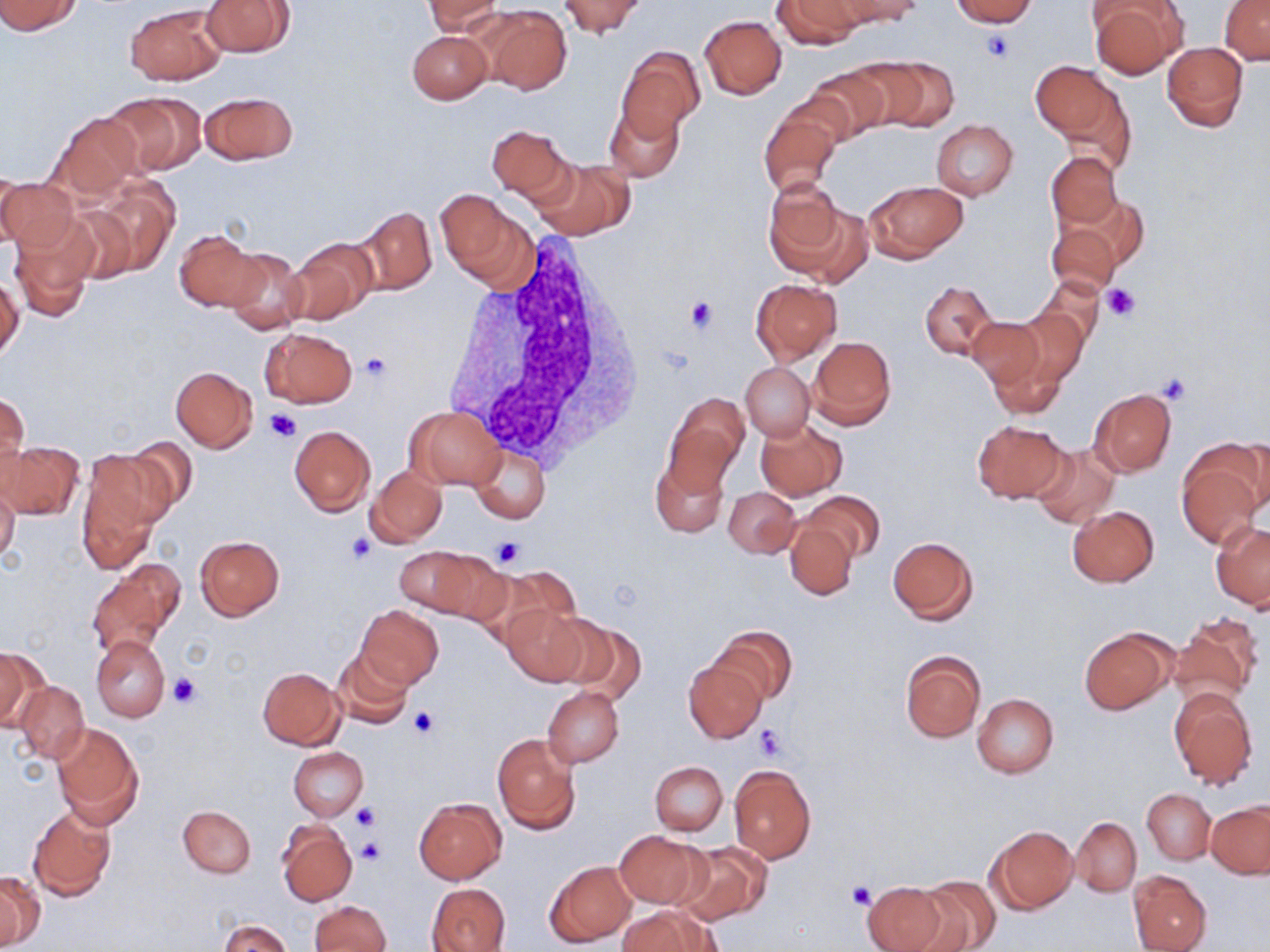

Summary:
  - Coordinate format: approximate bounding boxes as (x1, y1, x2, y2) in pixels
  - Uninfected red blood cell locations: (0, 0, 83, 35), (199, 0, 294, 57), (425, 0, 503, 37), (560, 0, 644, 37), (773, 0, 864, 48), (838, 0, 924, 26), (950, 0, 1037, 26), (1087, 1, 1185, 80), (1219, 1, 1270, 64), (125, 3, 227, 85), (482, 6, 570, 93), (698, 15, 786, 100), (406, 30, 491, 105), (1161, 42, 1248, 132), (617, 48, 704, 140), (857, 58, 957, 130), (1031, 61, 1118, 140), (804, 66, 889, 141), (1056, 74, 1139, 173), (102, 90, 206, 175), (198, 90, 298, 166), (604, 101, 683, 183), (758, 108, 840, 199), (48, 112, 143, 200), (930, 119, 1019, 200), (486, 123, 574, 203), (1046, 151, 1122, 230), (534, 159, 634, 240), (0, 173, 77, 257), (88, 179, 179, 274), (764, 180, 846, 276), (864, 180, 966, 262), (436, 189, 533, 287), (61, 203, 138, 286), (353, 206, 437, 295), (1046, 214, 1126, 297), (9, 216, 96, 322), (177, 230, 264, 314), (284, 237, 377, 327), (219, 244, 309, 335), (0, 275, 23, 364), (1032, 278, 1107, 349), (751, 279, 842, 362), (921, 280, 997, 361), (1009, 308, 1087, 387), (966, 317, 1044, 388), (260, 328, 357, 408), (809, 336, 896, 430), (986, 342, 1068, 420), (742, 363, 813, 440), (170, 367, 258, 452), (1088, 387, 1176, 477), (1, 390, 29, 482), (665, 394, 749, 490), (406, 405, 505, 490), (756, 419, 847, 499), (971, 420, 1068, 503), (288, 425, 375, 516), (124, 436, 200, 516), (1227, 439, 1270, 516), (2, 441, 84, 519), (1029, 442, 1121, 528), (471, 445, 550, 524), (77, 449, 165, 568), (1177, 451, 1265, 551), (650, 455, 728, 536), (365, 466, 447, 548), (0, 479, 20, 566), (724, 486, 800, 558), (802, 490, 883, 565), (1067, 505, 1160, 588), (785, 520, 856, 599), (1212, 522, 1269, 610), (194, 535, 285, 621), (887, 535, 979, 624), (394, 546, 488, 616), (426, 553, 512, 629), (89, 562, 181, 654), (481, 567, 580, 649), (356, 604, 444, 689), (501, 604, 588, 685), (551, 615, 644, 701), (1169, 616, 1261, 707), (710, 626, 797, 704), (1079, 627, 1175, 713), (91, 635, 171, 722), (0, 645, 41, 730), (333, 650, 415, 728), (900, 651, 985, 742), (685, 659, 767, 742), (257, 666, 345, 749), (15, 681, 90, 765), (543, 686, 623, 767), (1168, 686, 1257, 790), (972, 693, 1059, 778), (50, 722, 144, 827), (492, 733, 581, 835), (289, 746, 368, 821), (650, 760, 727, 835), (729, 765, 815, 863), (1143, 788, 1215, 863), (415, 798, 506, 883), (1206, 801, 1270, 879), (178, 805, 256, 877), (28, 808, 116, 901), (1071, 817, 1141, 896), (277, 820, 357, 907), (988, 825, 1077, 914), (614, 830, 706, 908), (674, 840, 771, 925), (546, 860, 637, 946), (1128, 871, 1211, 952), (0, 873, 44, 949), (914, 876, 1000, 952), (861, 879, 951, 952), (427, 883, 511, 952), (310, 900, 391, 952), (617, 907, 715, 952), (218, 919, 291, 952)
  - Platelet locations: (983, 31, 1014, 63), (1103, 284, 1141, 321), (684, 296, 717, 333), (360, 353, 392, 383), (1156, 373, 1192, 406), (266, 408, 301, 442), (344, 532, 378, 567), (490, 536, 525, 569), (170, 673, 202, 709), (408, 707, 441, 739), (753, 725, 786, 760), (351, 804, 379, 831), (355, 837, 385, 866), (846, 882, 876, 909)
  - White blood cell locations: (441, 242, 642, 466)
  - Slide-level diagnosis: negative for blood parasites
  - Stain: May-Grünwald-Giemsa
  - Modality: optical microscopy
  - Preparation: thin blood film
  - Image size: 1270×952 pixels
  - Magnification: 1000x
  - Field of view: one of a larger specimen